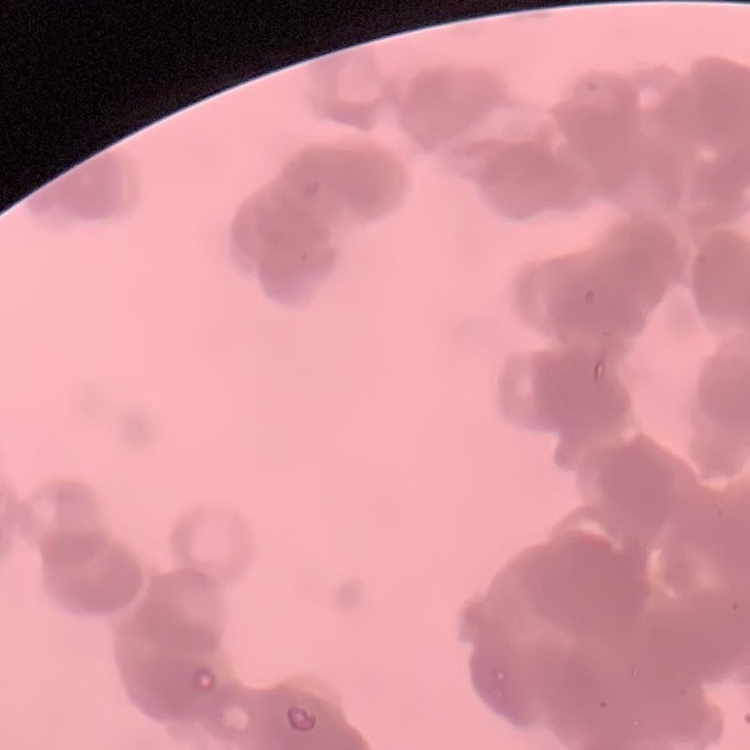
red blood cell morphology = rouleaux formation
preparation = thin blood film
image type = one tile cut from a larger photomicrograph
stain = Field's or Giemsa